State which cell type is depicted.
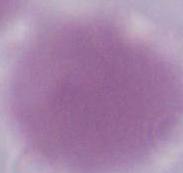
An erythrocyte.

Summary:
  - Modality: photomicrograph
  - Magnification: 1000x